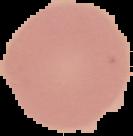

Summary:
  - Preparation: thin blood smear
  - Image size: 133×136 pixels
  - Malaria status: uninfected
  - Image type: cell region segmented out of the field of view; surrounding area masked to black